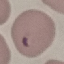
result = malaria parasites identified
stain = Giemsa
image type = cell patch, automatically extracted from a larger field of view and resized to 64 × 64 pixels
capture = smartphone camera at the microscope eyepiece
preparation = thin blood smear